Report the malaria status of this cell.
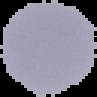

Uninfected.

image_type: cell region segmented out of the field of view; surrounding area masked to black
image_size: 97×97 pixels
preparation: thin blood film